Locate every blood parasite and identify its species.
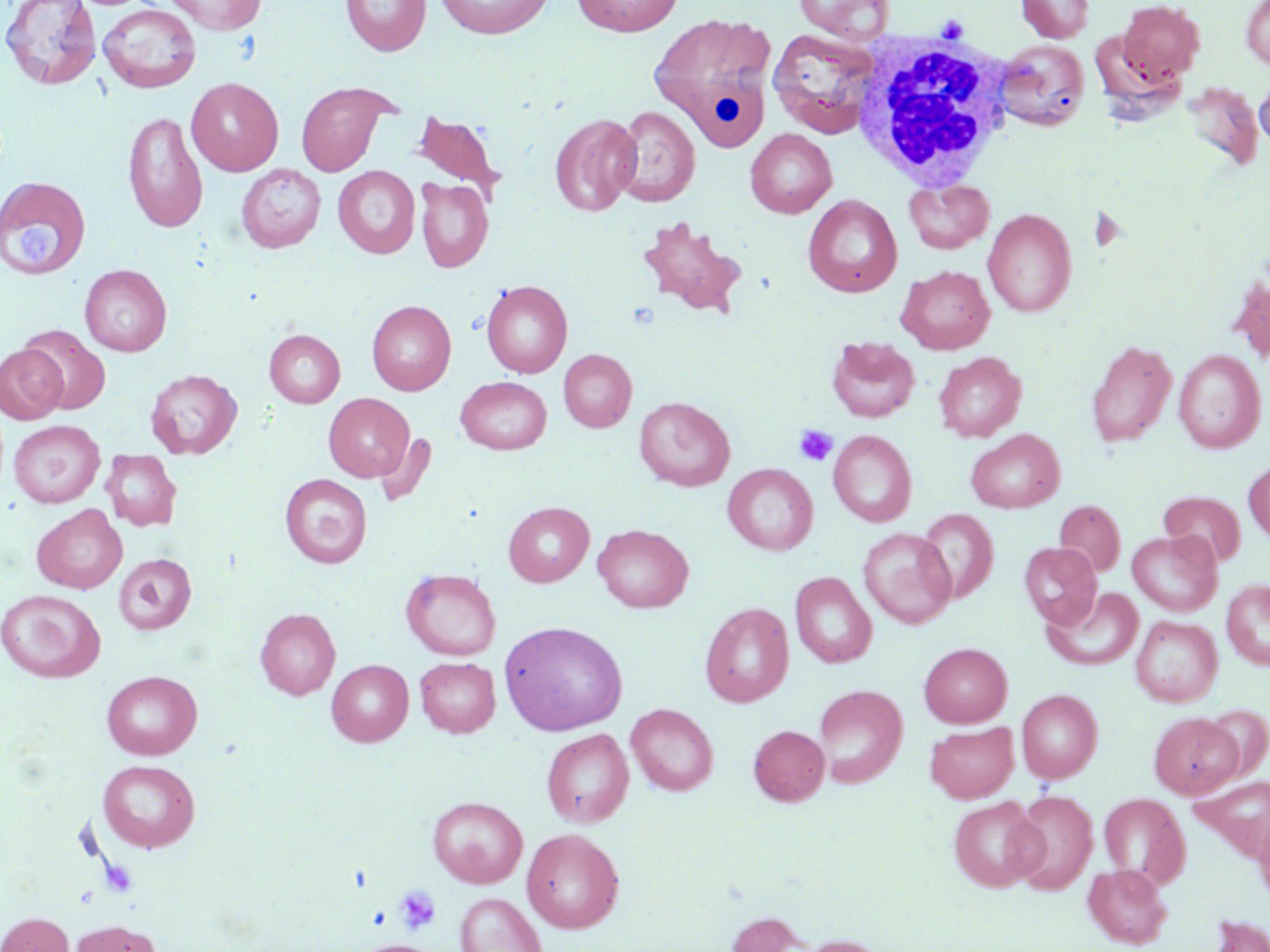
No blood parasites observed.

Approximate bounding boxes as named x1/y1/x2/y2 corners in pixels. Platelet locations: (x1=937, y1=15, x2=968, y2=40), (x1=11, y1=221, x2=67, y2=267), (x1=794, y1=424, x2=838, y2=467), (x1=394, y1=884, x2=441, y2=935). Uninfected red blood cell locations: (x1=1, y1=0, x2=101, y2=90), (x1=166, y1=0, x2=266, y2=34), (x1=341, y1=0, x2=430, y2=56), (x1=435, y1=0, x2=554, y2=38), (x1=573, y1=0, x2=683, y2=36), (x1=793, y1=0, x2=894, y2=44), (x1=1017, y1=0, x2=1093, y2=43), (x1=1117, y1=0, x2=1205, y2=84), (x1=1241, y1=1, x2=1270, y2=71), (x1=98, y1=3, x2=201, y2=93), (x1=648, y1=11, x2=778, y2=147), (x1=767, y1=28, x2=882, y2=139), (x1=995, y1=40, x2=1089, y2=131), (x1=1254, y1=70, x2=1270, y2=151), (x1=187, y1=77, x2=283, y2=175), (x1=296, y1=81, x2=391, y2=176), (x1=1180, y1=81, x2=1263, y2=171), (x1=612, y1=105, x2=700, y2=207), (x1=123, y1=110, x2=208, y2=233), (x1=411, y1=110, x2=507, y2=199), (x1=549, y1=114, x2=641, y2=216), (x1=745, y1=128, x2=837, y2=218), (x1=236, y1=164, x2=326, y2=253), (x1=333, y1=166, x2=420, y2=258), (x1=0, y1=176, x2=91, y2=281), (x1=415, y1=178, x2=493, y2=272), (x1=904, y1=178, x2=995, y2=254), (x1=803, y1=194, x2=902, y2=297), (x1=983, y1=208, x2=1076, y2=317), (x1=637, y1=217, x2=748, y2=318), (x1=80, y1=264, x2=172, y2=356), (x1=897, y1=265, x2=995, y2=354), (x1=1228, y1=276, x2=1270, y2=365), (x1=481, y1=280, x2=572, y2=378), (x1=367, y1=300, x2=456, y2=395), (x1=18, y1=325, x2=110, y2=414), (x1=265, y1=329, x2=345, y2=407), (x1=827, y1=336, x2=918, y2=423), (x1=1085, y1=339, x2=1177, y2=448), (x1=1, y1=344, x2=67, y2=423), (x1=558, y1=349, x2=637, y2=432), (x1=1174, y1=349, x2=1265, y2=452), (x1=934, y1=352, x2=1027, y2=441), (x1=146, y1=369, x2=242, y2=459), (x1=456, y1=376, x2=552, y2=454), (x1=324, y1=393, x2=414, y2=482), (x1=634, y1=396, x2=735, y2=491), (x1=9, y1=420, x2=105, y2=508), (x1=966, y1=428, x2=1065, y2=514), (x1=828, y1=430, x2=916, y2=527), (x1=373, y1=432, x2=437, y2=508), (x1=101, y1=450, x2=182, y2=531), (x1=1243, y1=459, x2=1270, y2=543), (x1=723, y1=463, x2=818, y2=555), (x1=280, y1=474, x2=372, y2=568), (x1=1159, y1=491, x2=1245, y2=567), (x1=1054, y1=500, x2=1125, y2=577), (x1=503, y1=501, x2=594, y2=587), (x1=32, y1=504, x2=127, y2=593), (x1=918, y1=508, x2=999, y2=604), (x1=593, y1=524, x2=693, y2=613), (x1=859, y1=527, x2=956, y2=628), (x1=1127, y1=530, x2=1222, y2=616), (x1=1019, y1=542, x2=1102, y2=628), (x1=113, y1=553, x2=196, y2=634), (x1=401, y1=568, x2=501, y2=659), (x1=790, y1=572, x2=877, y2=667), (x1=1221, y1=579, x2=1270, y2=670), (x1=1042, y1=586, x2=1144, y2=671), (x1=1, y1=589, x2=106, y2=683), (x1=700, y1=602, x2=793, y2=707), (x1=255, y1=608, x2=340, y2=700), (x1=1131, y1=615, x2=1222, y2=707), (x1=499, y1=620, x2=628, y2=735), (x1=919, y1=643, x2=1012, y2=727), (x1=415, y1=657, x2=500, y2=737), (x1=327, y1=660, x2=414, y2=746), (x1=102, y1=670, x2=202, y2=759), (x1=813, y1=684, x2=907, y2=788), (x1=1016, y1=689, x2=1103, y2=783), (x1=626, y1=703, x2=718, y2=795), (x1=1200, y1=705, x2=1269, y2=779), (x1=1149, y1=712, x2=1243, y2=798), (x1=925, y1=722, x2=1018, y2=802), (x1=749, y1=725, x2=830, y2=805), (x1=542, y1=728, x2=634, y2=828), (x1=98, y1=760, x2=200, y2=852), (x1=1194, y1=776, x2=1270, y2=860), (x1=1010, y1=790, x2=1098, y2=895), (x1=1100, y1=793, x2=1189, y2=886), (x1=427, y1=796, x2=528, y2=888), (x1=948, y1=796, x2=1045, y2=892), (x1=1254, y1=817, x2=1270, y2=907), (x1=522, y1=827, x2=625, y2=933), (x1=1083, y1=863, x2=1172, y2=949), (x1=455, y1=892, x2=547, y2=952), (x1=726, y1=911, x2=809, y2=952), (x1=0, y1=912, x2=73, y2=952), (x1=1206, y1=914, x2=1270, y2=952), (x1=68, y1=920, x2=162, y2=952), (x1=797, y1=935, x2=887, y2=952), (x1=356, y1=940, x2=443, y2=952). White blood cell locations: (x1=849, y1=34, x2=1016, y2=190). Slide-level diagnosis: negative for blood parasites. One field of a larger specimen. Captured at 1000x magnification. May-Grünwald-Giemsa-stained preparation. Light microscopy. Thin blood smear. Image is 1270×952 pixels.